Identify the cell.
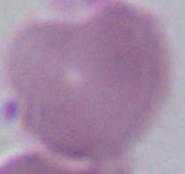

An erythrocyte.

Summary:
  - Modality: photomicrograph
  - Magnification: 1000x